Point out each leukocyte.
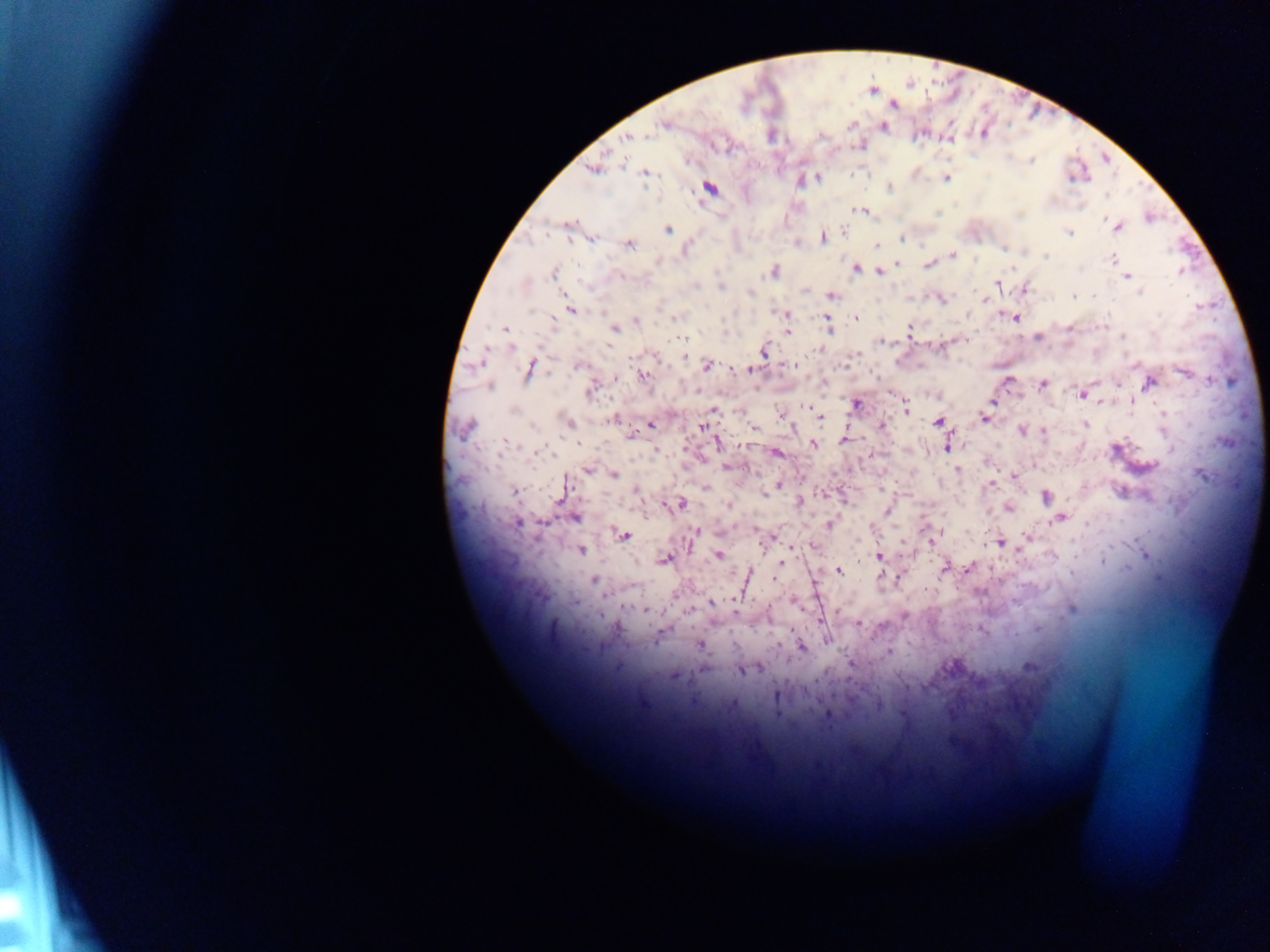

No leukocytes observed.

Approximate centers as [x, y] in pixels. Plasmodium parasite locations: [893, 105], [663, 125], [884, 126], [628, 137], [645, 137], [950, 139], [859, 146], [623, 163], [593, 170], [646, 173], [818, 177], [947, 178], [890, 188], [709, 189], [862, 210], [568, 223], [1117, 226], [668, 229], [844, 231], [1069, 232], [823, 237], [902, 238], [591, 240], [629, 244], [876, 245], [1004, 248], [952, 255], [1046, 256], [1112, 259], [897, 263], [928, 265], [855, 268], [773, 271], [879, 271], [553, 273], [621, 276], [1127, 277], [997, 285], [695, 286], [720, 287], [1025, 289], [805, 291], [750, 293], [1140, 293], [831, 295], [1074, 295], [1094, 295], [942, 300], [571, 309], [779, 312], [968, 315], [677, 317], [1014, 317], [856, 319], [636, 320], [554, 321], [828, 325], [504, 328], [614, 329], [787, 331], [910, 331], [1036, 337], [1123, 338], [682, 339], [943, 346], [511, 348], [817, 350], [765, 351], [579, 365], [795, 365], [707, 366], [531, 369], [749, 370], [1186, 373], [643, 376], [1150, 383], [1043, 384], [490, 386], [591, 389], [1082, 394], [992, 402], [855, 404], [906, 408], [713, 410], [821, 418], [984, 418], [611, 420], [569, 422], [938, 422], [1086, 424], [650, 425], [702, 426], [881, 426], [466, 428], [753, 428], [1022, 430], [1044, 432], [631, 436], [844, 440], [717, 443], [814, 445], [948, 445], [1117, 449], [539, 452], [777, 454], [728, 466], [1145, 467], [957, 469], [587, 470], [614, 474], [1203, 475], [1014, 476], [777, 485], [991, 485], [706, 488], [881, 489], [636, 491], [515, 492], [768, 492], [1045, 497], [560, 499], [800, 502], [680, 505], [728, 506], [1007, 508], [887, 510], [575, 518], [1060, 518], [517, 523], [831, 523], [697, 532], [622, 535], [767, 538], [1028, 538], [930, 540], [1000, 543], [581, 550], [1145, 554], [718, 555], [880, 557], [665, 559], [781, 563], [969, 567], [945, 568], [839, 570], [880, 576], [775, 577], [898, 577], [595, 580], [711, 603], [646, 610], [1072, 610], [736, 612], [859, 624], [881, 627], [827, 640], [700, 645], [801, 646], [888, 652], [1029, 667], [758, 669], [741, 671], [673, 675], [777, 696], [827, 715]. Mobile-phone photograph taken through the microscope. Thick blood smear. Image is 1270×952 pixels. Single field of view. Sample from Ghana.